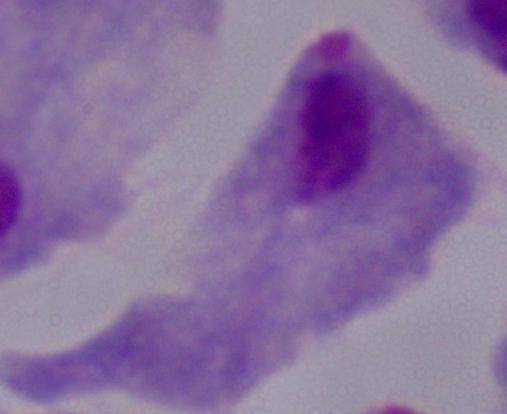

Summary:
  - Modality: photomicrograph
  - Identification: trichomonad
  - Magnification: 1000x